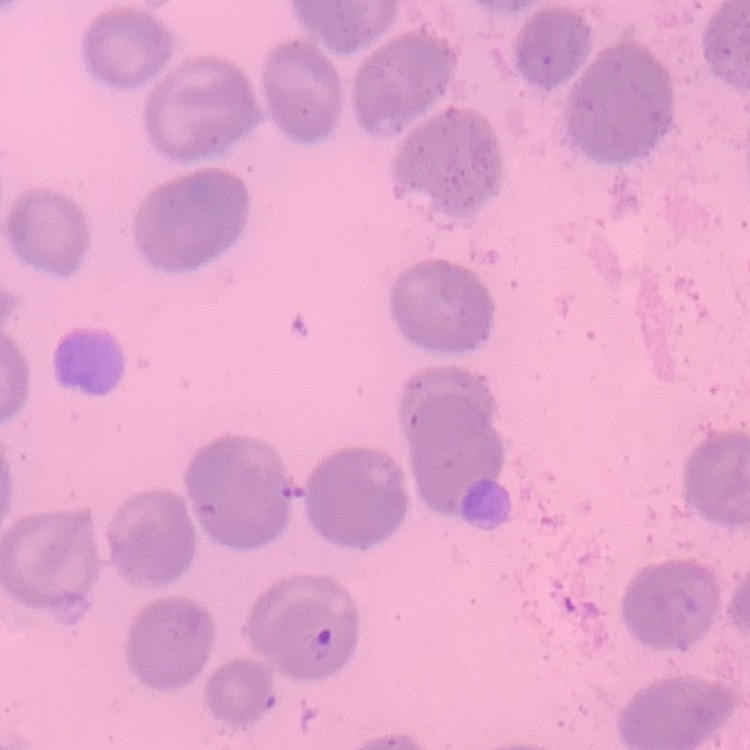 The red blood cells show no rouleaux formation. Thin blood film. One tile cut from a larger photomicrograph. Stained with either Field's or Giemsa.